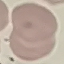

{
  "malaria_status": "uninfected",
  "capture": "smartphone camera at the microscope eyepiece",
  "stain": "Giemsa",
  "image_type": "automatically extracted cell patch, resized to 64 × 64 pixels",
  "preparation": "thin blood film"
}